Give a bounding box for every leukocyte visible.
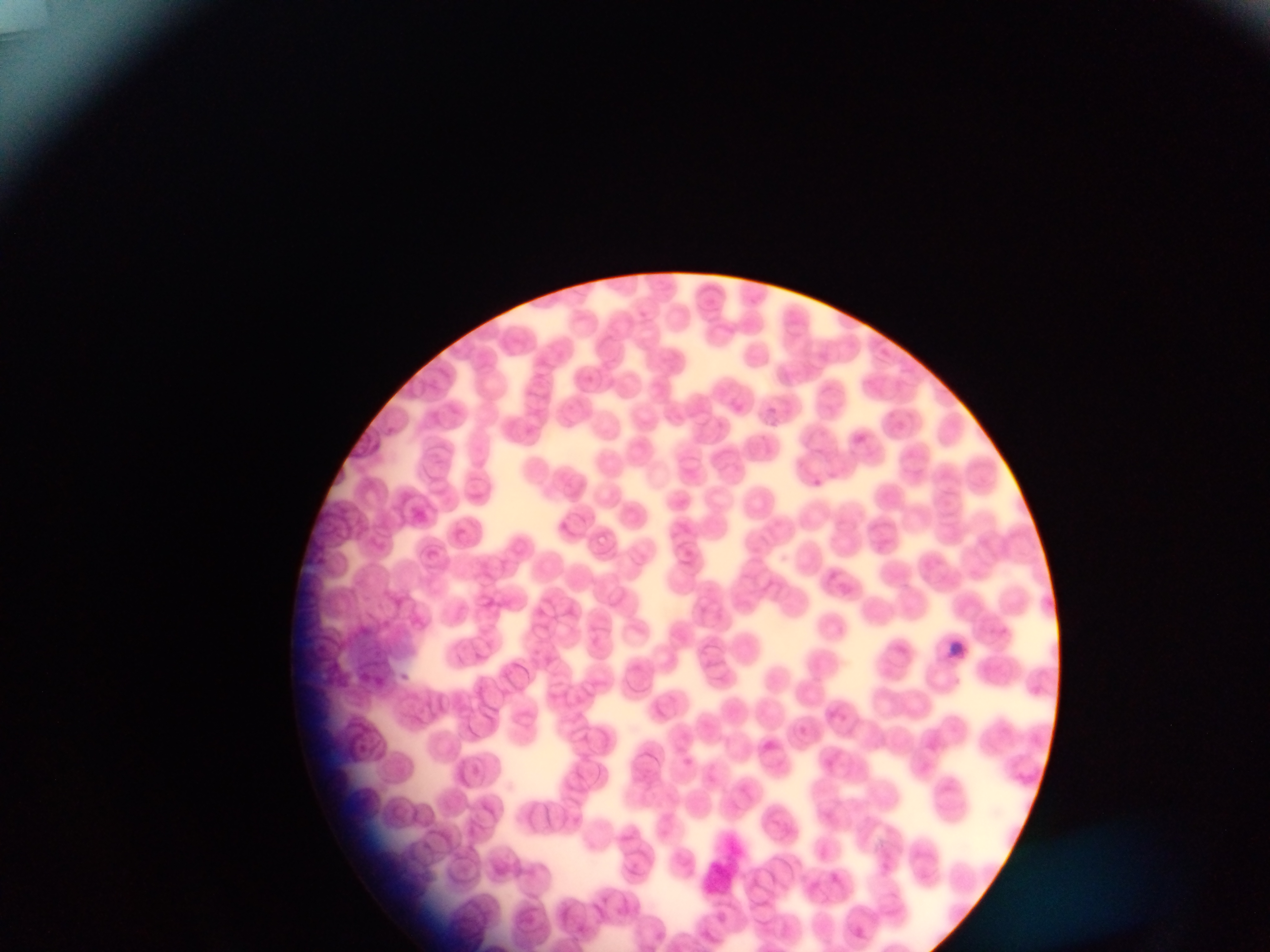
No leukocytes observed.

image size = 1270×952 pixels
country = Ghana
capture = mobile-phone photograph through a microscope
field of view = single
preparation = thin blood film
malaria parasite locations = approximate bounding boxes as left top right bottom in pixels: 811 475 820 489; 1000 623 1020 643; 943 638 968 653; 396 669 413 686